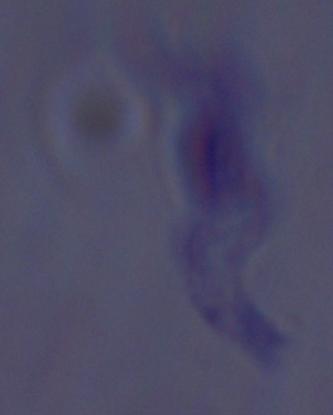

modality = photomicrograph
magnification = 1000x
identification = trypanosome